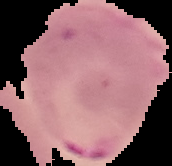
Cell region segmented out of the field of view; the surrounding area is masked to black. Result: Plasmodium parasites detected. From a thin blood film. Image is 172×166 pixels.